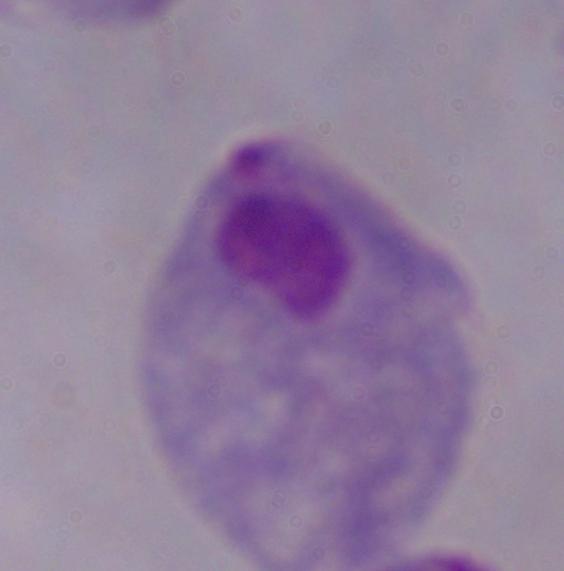 A trichomonad is seen. Photomicrograph. Captured at 1000x magnification.